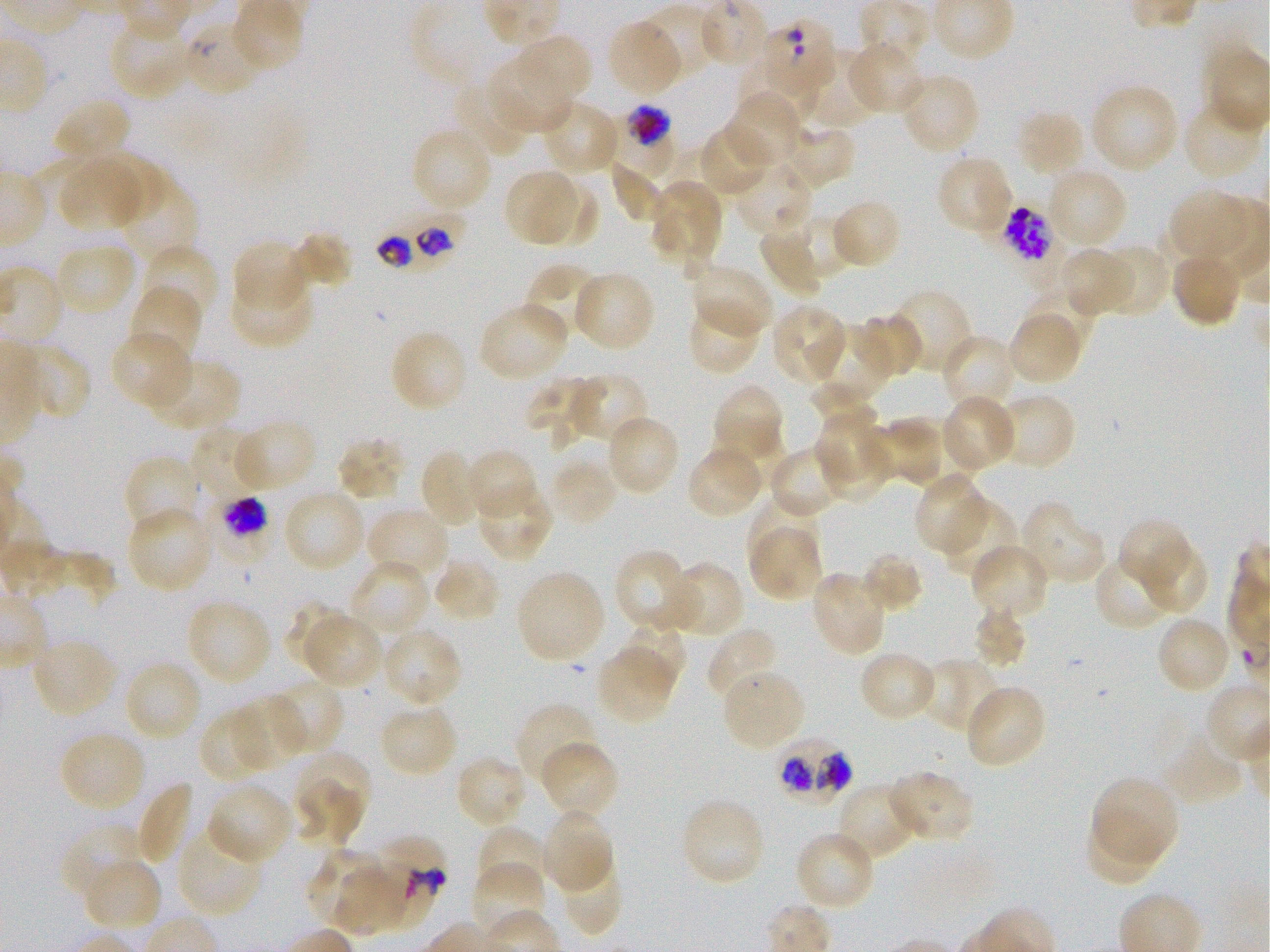

Not every red blood cell is marked. A life-cycle stage — or a range of stages, where the recorded stages span more than one — follows each staged infected red blood cell.
locations_of_infected_red_blood_cells: 'approximate bounding boxes as (x1, y1, x2, y2) in pixels: (611, 105, 674, 176) early trophozoite to early schizont; (982, 201, 1066, 287) schizont; (377, 220, 462, 270); (772, 734, 853, 800)'
field_of_view: one from this slide
donor_blood_group: O+
objective: 100x, oil immersion, numerical aperture 1.25
preparation: thin blood film
image_size: 1270×952 pixels
stain: Giemsa
locations_of_uninfected_red_blood_cells: 'approximate bounding boxes as (x1, y1, x2, y2) in pixels: (642, 4, 716, 83), (108, 17, 194, 100), (607, 20, 684, 96), (514, 31, 592, 105), (848, 41, 923, 115), (736, 47, 811, 125), (798, 48, 881, 130), (488, 58, 572, 134), (899, 72, 981, 155), (452, 80, 534, 158), (1089, 83, 1180, 173), (726, 93, 802, 170), (52, 97, 132, 164), (1183, 97, 1264, 181), (540, 99, 621, 175), (1015, 109, 1086, 179), (700, 122, 772, 198), (777, 123, 856, 190), (410, 126, 493, 213), (673, 146, 737, 216), (93, 152, 167, 220), (936, 154, 1013, 236), (57, 157, 143, 232), (732, 160, 813, 238), (610, 163, 664, 221), (1046, 167, 1128, 250), (504, 170, 581, 245), (119, 175, 198, 264), (542, 178, 598, 248), (649, 180, 723, 263), (1169, 189, 1248, 258), (830, 199, 903, 269), (795, 212, 854, 277), (762, 229, 824, 301), (289, 231, 353, 291), (232, 240, 309, 312), (54, 242, 136, 316), (143, 244, 220, 323), (1096, 244, 1169, 319), (1058, 246, 1137, 316), (1170, 252, 1243, 328), (525, 263, 601, 337), (690, 263, 773, 337), (544, 266, 628, 347), (572, 269, 656, 352), (230, 276, 316, 347), (1021, 285, 1099, 355), (128, 286, 203, 365), (886, 288, 975, 376), (684, 300, 761, 375), (479, 301, 570, 382), (770, 303, 848, 384), (1008, 311, 1083, 384), (856, 313, 922, 379), (809, 322, 894, 407), (389, 329, 468, 413), (110, 331, 193, 410), (941, 334, 1017, 413), (16, 343, 91, 422), (147, 357, 242, 431), (566, 374, 650, 448), (523, 375, 595, 446), (810, 381, 877, 428), (712, 383, 786, 466), (995, 392, 1076, 472), (941, 395, 1018, 473), (815, 410, 890, 491), (605, 414, 680, 497), (232, 419, 317, 492), (866, 420, 943, 487), (191, 425, 269, 501), (335, 435, 408, 502), (685, 444, 765, 520), (767, 446, 845, 518), (419, 448, 483, 529), (466, 449, 539, 521), (122, 455, 203, 535), (549, 455, 618, 526), (914, 471, 987, 555), (476, 483, 554, 562), (282, 488, 366, 573), (747, 495, 821, 566), (943, 501, 1020, 581), (1020, 501, 1107, 584), (126, 507, 213, 594), (366, 507, 450, 586), (1119, 517, 1191, 593), (748, 524, 823, 602), (1138, 539, 1209, 617), (970, 544, 1051, 619), (612, 550, 695, 632), (858, 550, 924, 614), (1094, 552, 1175, 632), (346, 558, 432, 639), (431, 558, 503, 623), (665, 562, 744, 639), (516, 570, 606, 663), (810, 571, 887, 657), (186, 598, 272, 685), (283, 600, 351, 666), (972, 605, 1028, 670), (303, 612, 383, 690), (1155, 616, 1232, 695), (617, 623, 686, 695), (707, 627, 782, 704), (382, 628, 463, 707), (30, 638, 118, 718), (596, 647, 675, 723), (857, 650, 938, 723), (922, 657, 1002, 735), (122, 659, 203, 742), (721, 669, 806, 752), (269, 678, 345, 757), (964, 685, 1048, 770), (235, 696, 306, 770), (515, 702, 598, 787), (378, 703, 459, 778), (198, 708, 273, 785), (59, 730, 147, 812), (1160, 733, 1246, 805), (540, 741, 620, 820), (296, 751, 370, 829), (456, 754, 528, 830), (887, 770, 975, 843), (1093, 775, 1179, 865), (135, 780, 195, 865), (836, 782, 919, 863), (206, 783, 293, 865), (293, 787, 360, 847), (680, 797, 766, 887), (541, 809, 614, 894), (1086, 814, 1161, 887), (62, 823, 144, 901), (475, 826, 549, 898), (176, 827, 265, 918), (794, 830, 877, 911), (303, 847, 391, 930), (557, 857, 624, 938), (84, 858, 162, 933), (336, 863, 410, 940), (474, 863, 546, 939)'
culture: in-vitro P. falciparum strain 3D7, static
locations_of_red_blood_cells_of_indeterminate_infection_status: 'approximate bounding boxes as (x1, y1, x2, y2) in pixels: (761, 20, 838, 94), (185, 25, 261, 93), (216, 496, 269, 544), (374, 836, 446, 928)'